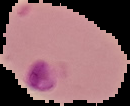 Segmented cell region on a black background. Result: malaria parasites detected. Image is 130×106 pixels. From a thin blood film.